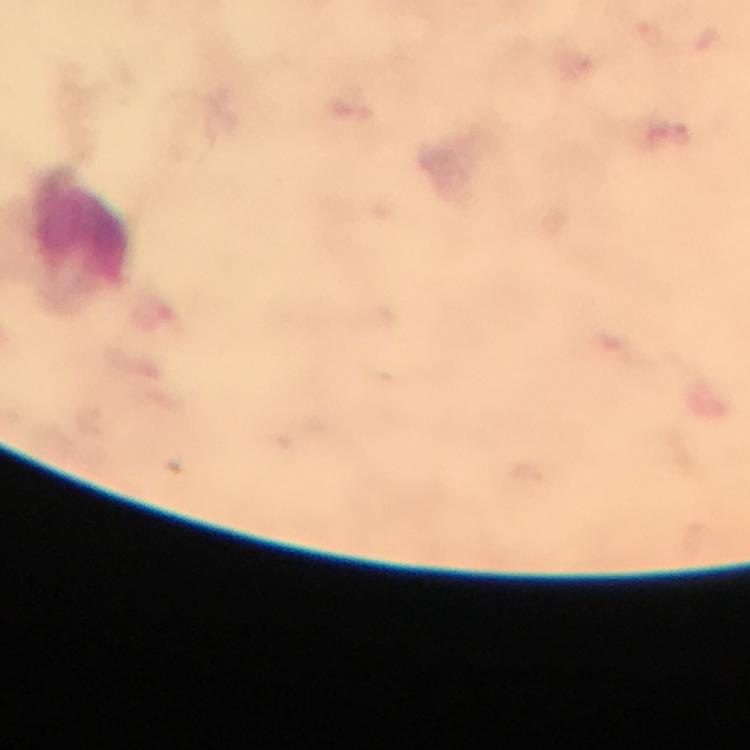
Approximate object centers, in pixels from the top-left corner. Plasmodium parasite locations: (x=681, y=133). Leukocyte locations: (x=82, y=237). Cropped region of a single field of view. At 100x magnification. From a diagnostic examination for malaria. Image is 750×750 pixels. Thick smear. Immersion oil was used. Giemsa stain. Smartphone photograph taken through a microscope.